State which parasite is depicted.
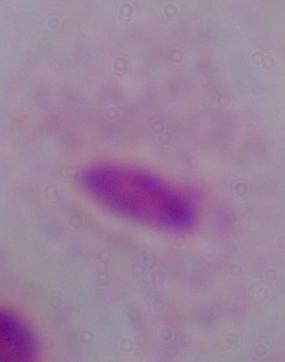

A trichomonad.

Captured at 1000x magnification. Photomicrograph.